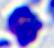

Summary:
  - Identification: leukocyte
  - Magnification: 400x
  - Modality: micrograph